Identify the preparation type.
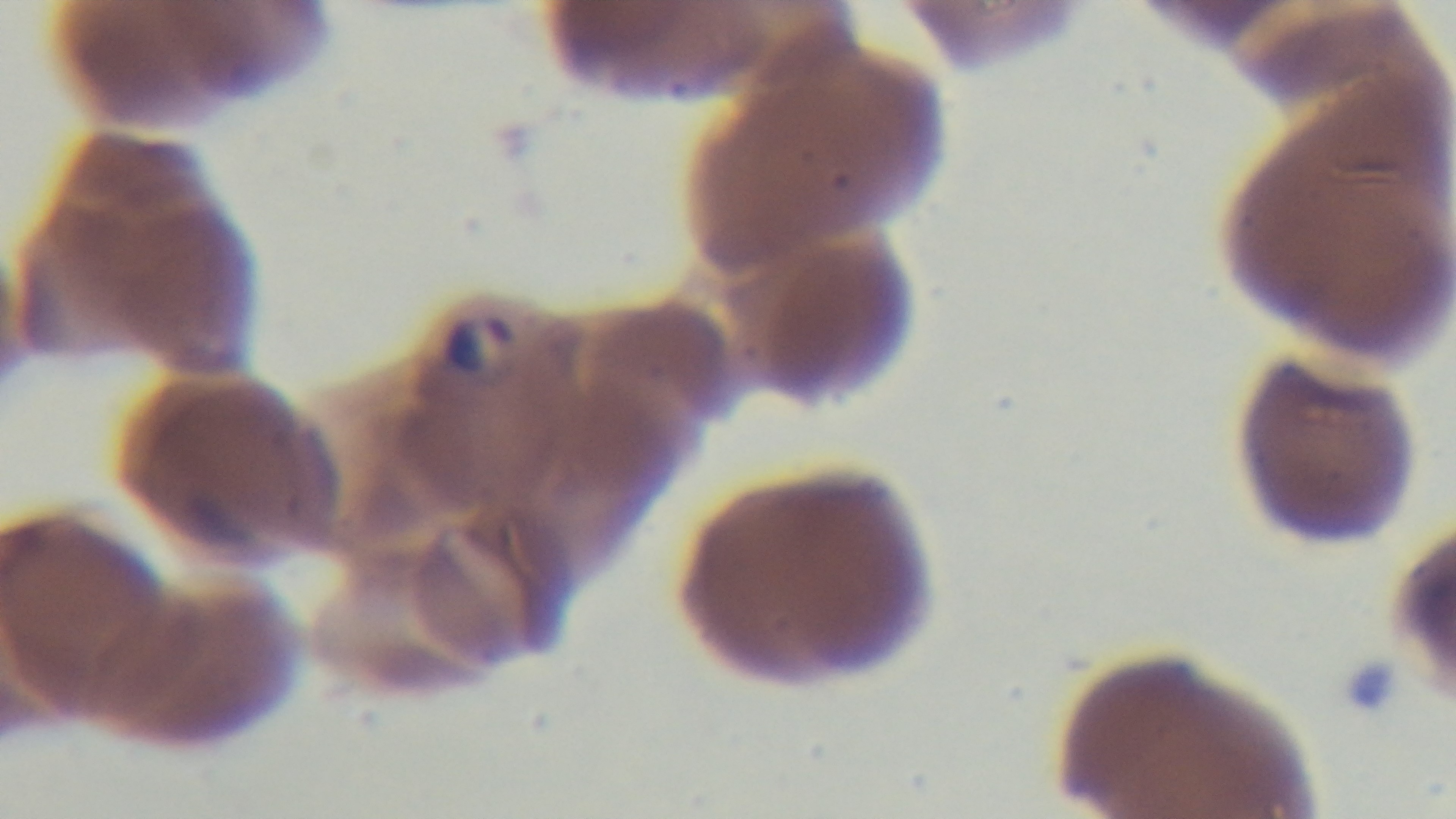
Thin.

stain: Giemsa
modality: light microscopy
objective: 100x oil immersion
capture: mounted 4K digital camera
field_of_view: one from the slide
malaria_status: infected